Identify the parasite.
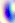
This is Toxoplasma gondii.

Captured at 400x magnification. Micrograph.